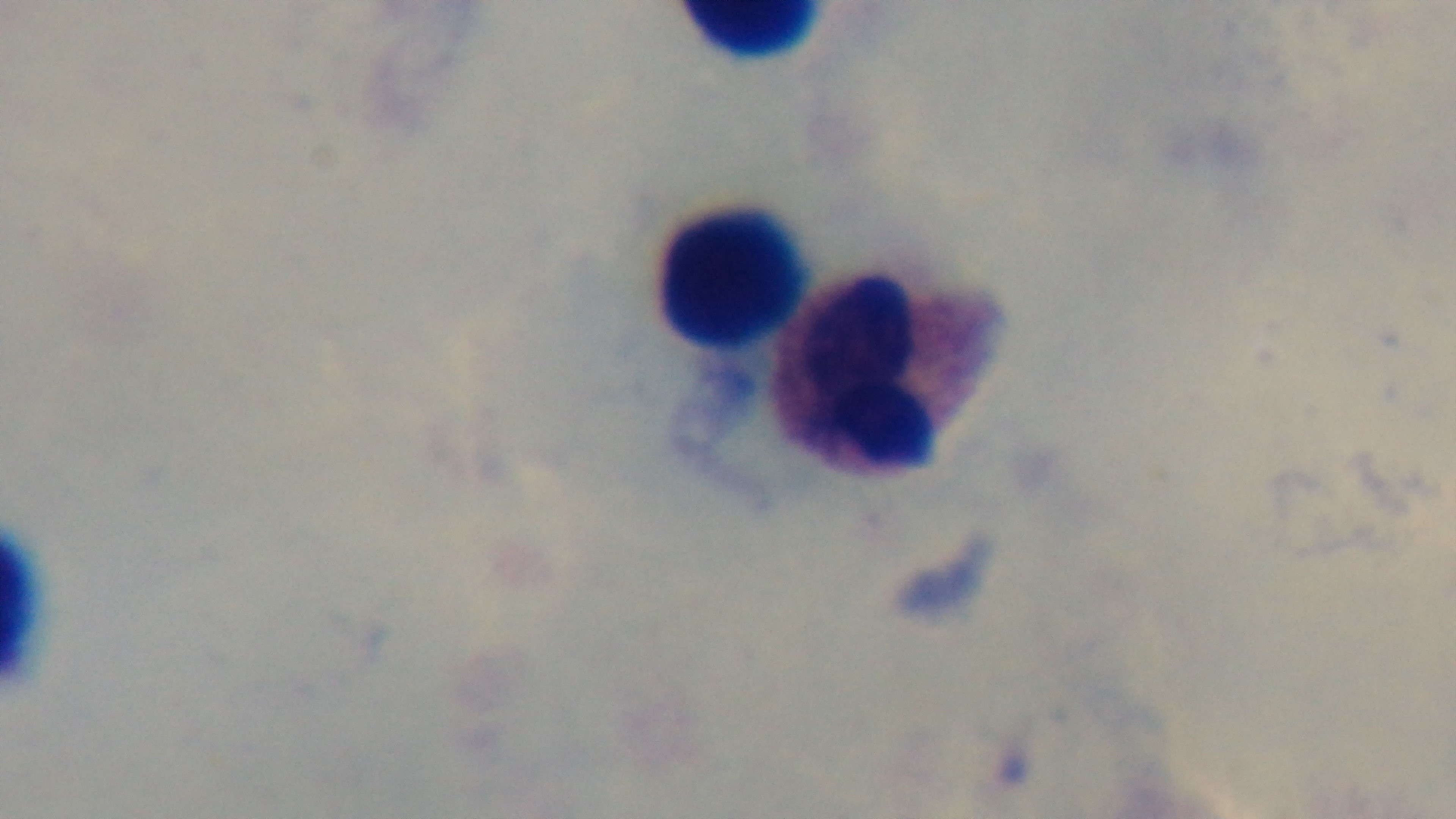
malaria_status: uninfected
modality: light microscopy
capture: mounted 4K digital camera
objective: 100x oil immersion
field_of_view: one from the slide
stain: Giemsa
preparation: thick smear